State the blood parasite species.
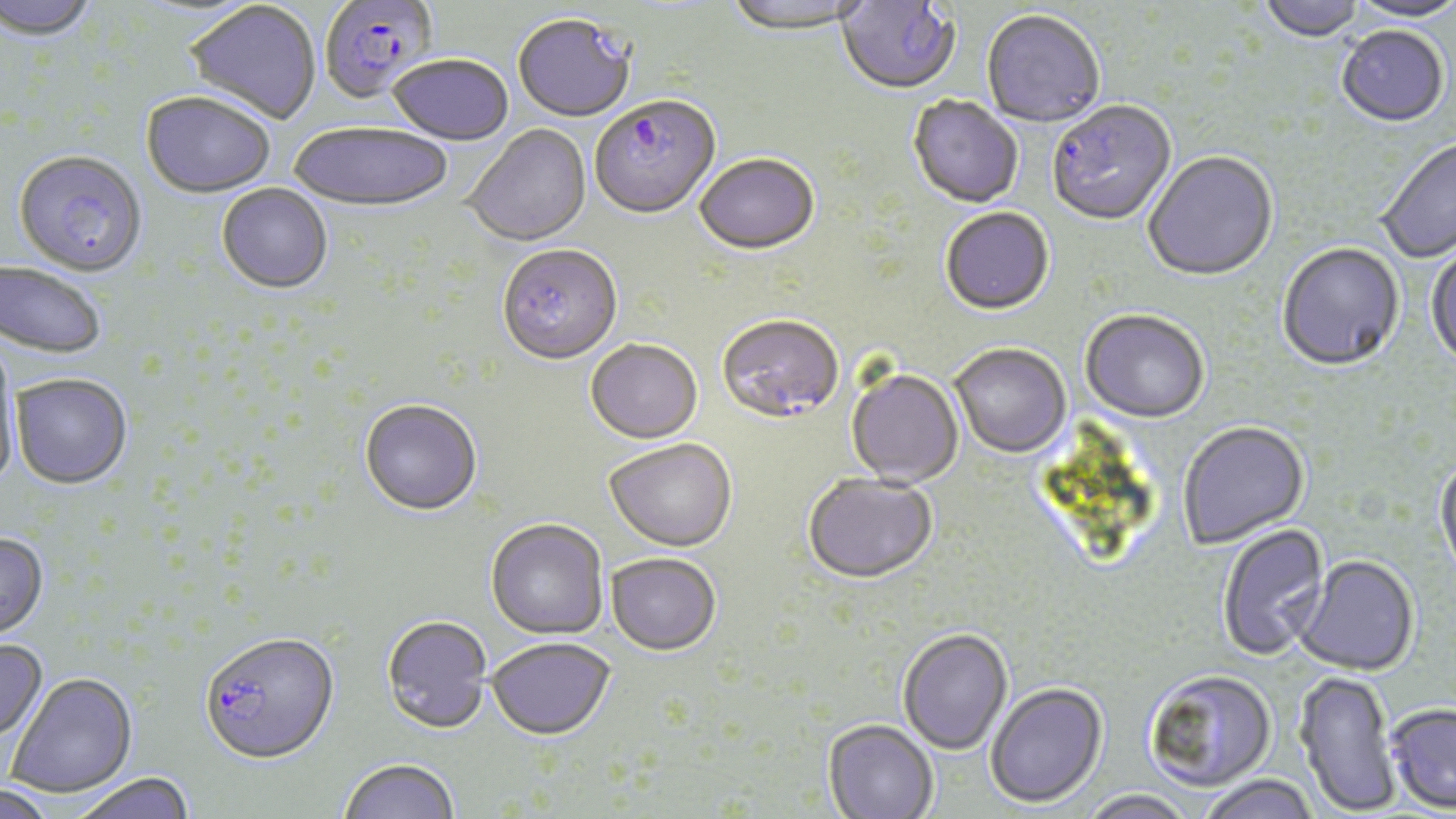

Plasmodium falciparum.

Summary:
  - Coordinate format: approximate bounding boxes as (x1,y1)-(x2,y2) corner pairs in pixels
  - Uninfected red blood cell locations: (0,0)-(101,44), (722,0)-(874,38), (1259,0)-(1366,44), (1346,0)-(1456,24), (183,2)-(321,126), (982,12)-(1105,130), (513,17)-(635,124), (1336,28)-(1449,129), (388,57)-(513,147), (141,94)-(275,200), (907,96)-(1023,210), (289,124)-(453,215), (464,126)-(592,249), (1375,138)-(1456,263), (1143,152)-(1279,284), (695,156)-(819,258), (216,184)-(333,296), (941,209)-(1054,317), (1277,244)-(1405,373), (1426,244)-(1456,372), (496,247)-(622,368), (0,262)-(106,361), (1080,311)-(1209,425), (586,341)-(703,446), (0,344)-(21,489), (950,345)-(1072,460), (845,369)-(964,488), (10,375)-(133,492), (359,401)-(482,518), (1178,423)-(1310,549), (604,441)-(737,554), (1434,456)-(1456,586), (802,475)-(937,587), (485,520)-(608,641), (1216,523)-(1331,661), (0,534)-(50,644), (606,555)-(721,657), (1293,557)-(1419,677), (380,617)-(492,736), (897,629)-(1013,755), (486,639)-(615,742), (0,641)-(49,746), (1143,670)-(1277,792), (1296,671)-(1401,816), (5,674)-(138,799), (985,684)-(1108,810), (1385,703)-(1456,813), (823,721)-(938,819), (339,760)-(459,819), (71,775)-(196,819), (1198,775)-(1320,819), (0,786)-(59,819), (1079,790)-(1196,819)
  - Plasmodium falciparum-infected red blood cell locations: (835,0)-(959,97), (319,2)-(439,107), (589,98)-(721,222), (1047,102)-(1177,228), (13,152)-(149,279), (717,316)-(843,427), (200,634)-(339,767)
  - Modality: light microscopy
  - Stain: May-Grünwald-Giemsa
  - Magnification: 1000x
  - Image size: 1456×819 pixels
  - Field of view: single
  - Preparation: thin blood smear